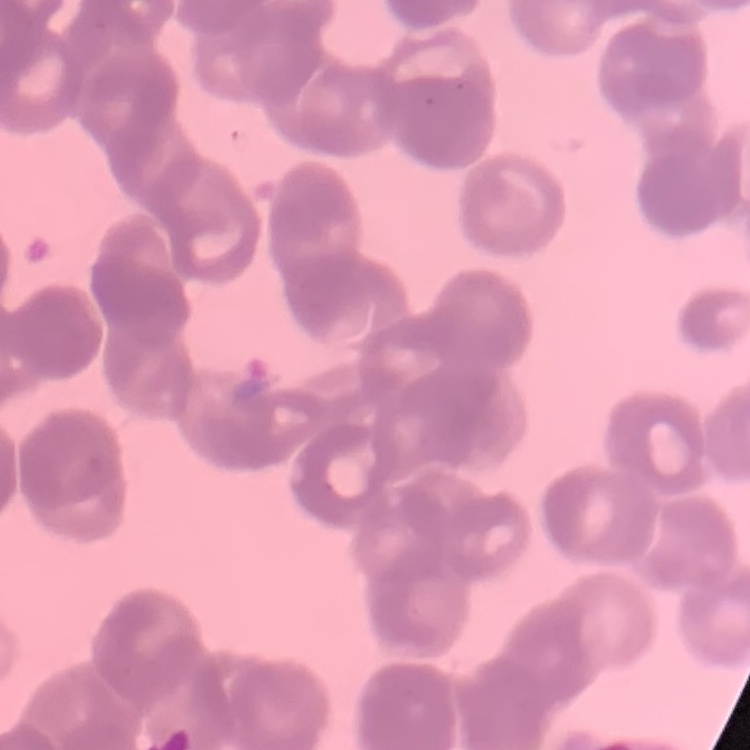 The erythrocytes show rouleaux formation. Field's or Giemsa stain. Thin blood smear. One tile cut from a larger photomicrograph.